Assess this cell for malaria.
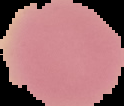

It is uninfected.

{
  "image_type": "cell region segmented out of the field of view; surrounding area masked to black",
  "image_size": "124×106 pixels",
  "preparation": "thin blood smear"
}